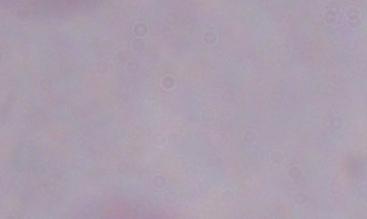
magnification = 1000x
modality = micrograph
identification = trypanosome